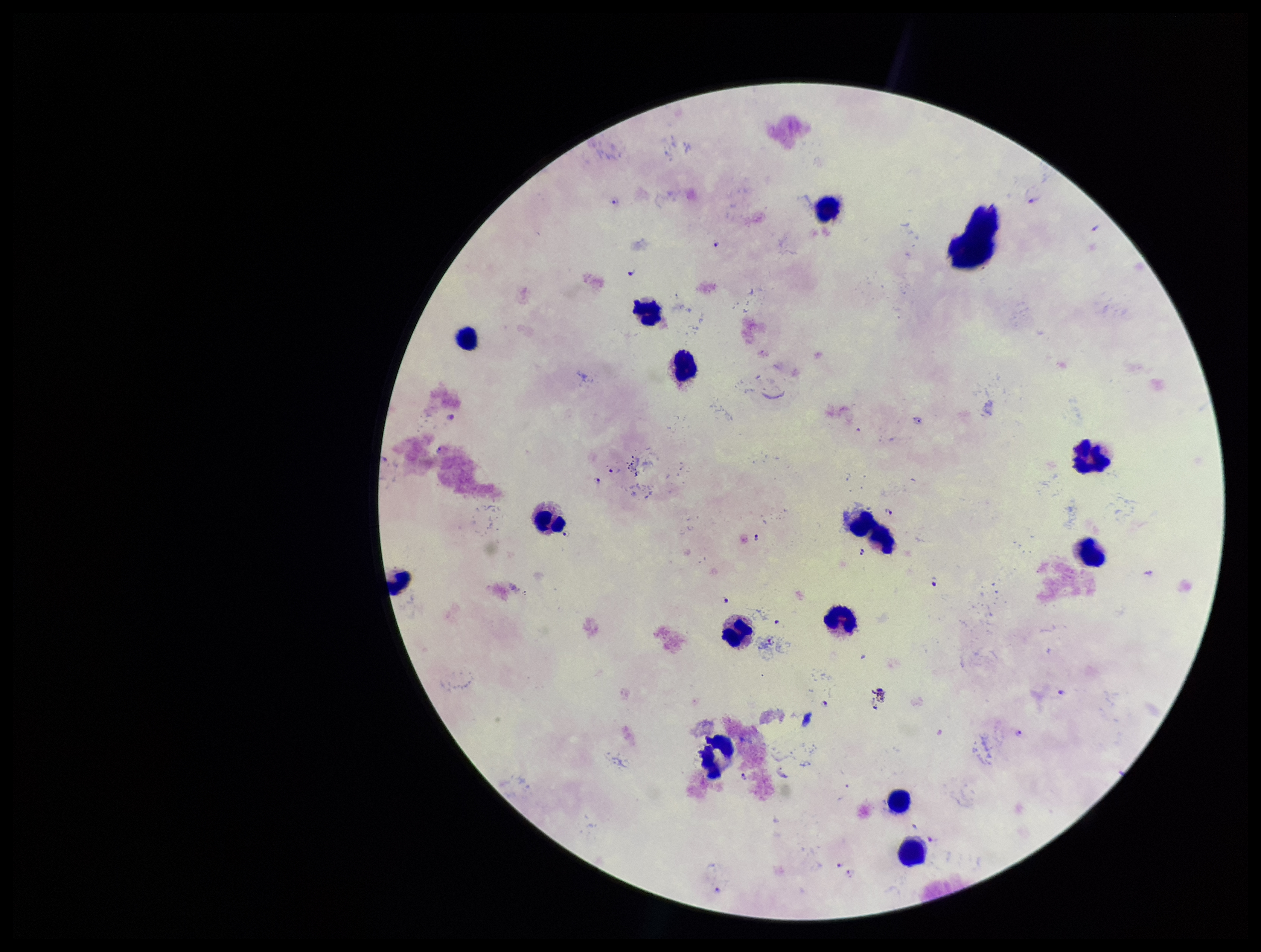

Leukocyte count: 15. Smartphone photograph taken through the eyepiece of a microscope. Patient malaria status: positive. Plasmodium parasites: identified. One field from this slide. Stained with Giemsa. Species reported for this patient: Plasmodium falciparum. Image is 1261×952 pixels. Parasite count: 13. Preparation: thick.